Locate every Plasmodium falciparum-infected red blood cell.
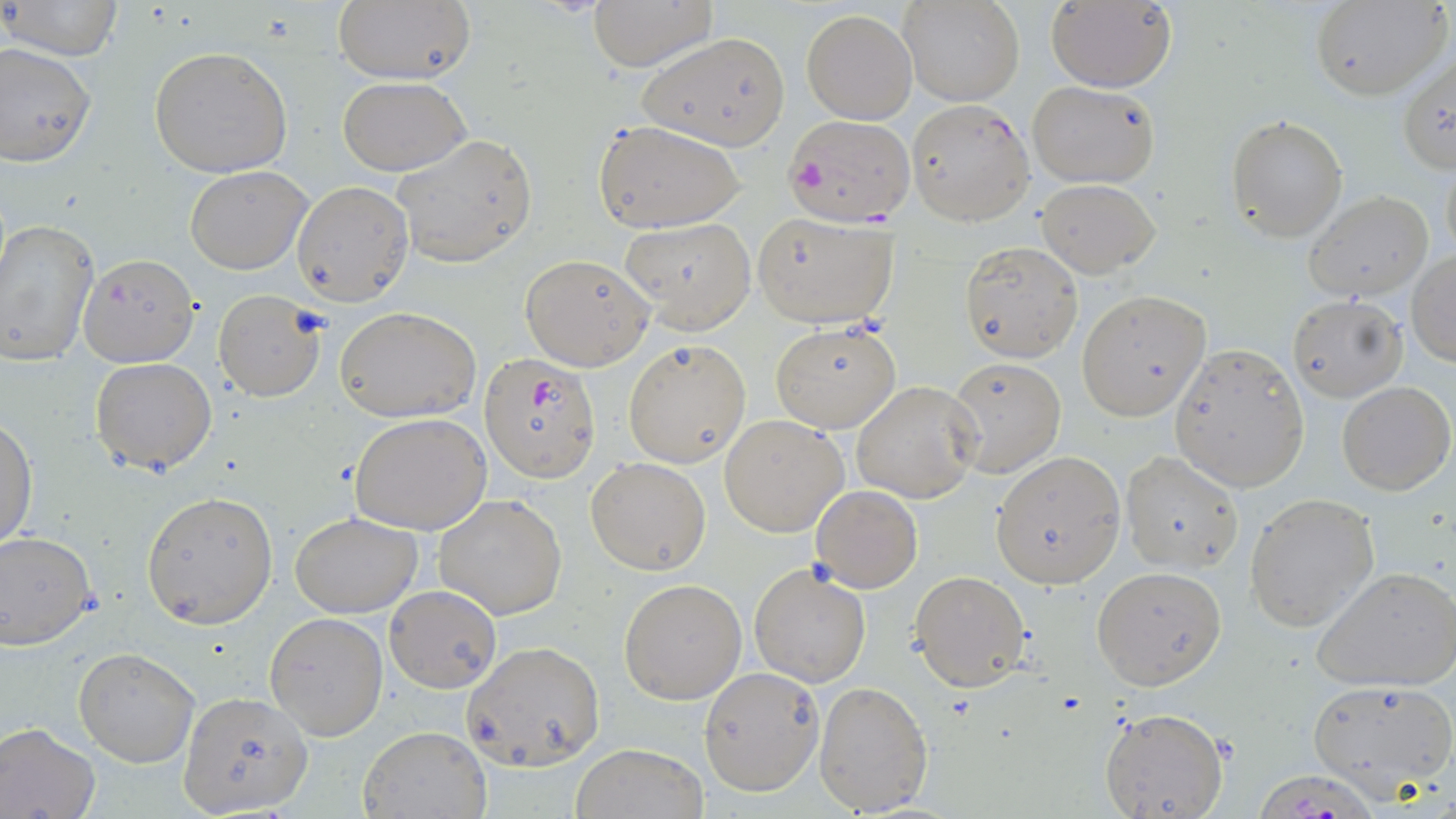

Approximate bounding boxes as (x1, y1, x2, y2) in pixels.
Plasmodium falciparum-infected red blood cells: (906, 99, 1034, 227), (783, 114, 915, 227), (480, 354, 600, 483).

Uninfected red blood cell locations: (330, 0, 477, 87), (584, 0, 718, 70), (901, 0, 1024, 107), (1309, 0, 1450, 102), (2, 1, 126, 62), (1045, 1, 1177, 91), (801, 7, 917, 125), (637, 30, 792, 152), (0, 42, 97, 166), (149, 44, 294, 177), (1397, 49, 1456, 176), (337, 76, 470, 175), (1026, 79, 1160, 188), (1226, 115, 1348, 241), (594, 120, 744, 233), (392, 133, 537, 268), (1440, 154, 1455, 265), (185, 166, 311, 274), (1037, 179, 1160, 276), (292, 180, 415, 305), (1304, 191, 1434, 302), (752, 211, 898, 329), (620, 218, 756, 332), (0, 219, 99, 369), (959, 240, 1084, 362), (1408, 250, 1456, 365), (78, 251, 199, 368), (519, 253, 654, 372), (213, 288, 326, 401), (1076, 290, 1211, 420), (1286, 294, 1405, 402), (334, 306, 480, 423), (769, 321, 902, 433), (622, 337, 751, 467), (1170, 345, 1310, 492), (90, 357, 218, 474), (947, 357, 1065, 477), (850, 380, 982, 502), (1338, 380, 1454, 496), (719, 413, 849, 537), (351, 414, 493, 534), (0, 419, 37, 552), (991, 451, 1124, 587), (1120, 451, 1245, 573), (585, 456, 712, 574), (811, 486, 924, 592), (141, 491, 278, 628), (1245, 493, 1380, 632), (431, 494, 569, 621), (289, 511, 422, 618), (0, 532, 98, 648), (749, 562, 872, 686), (1091, 566, 1227, 689), (1313, 566, 1456, 692), (910, 570, 1031, 691), (619, 577, 748, 704), (384, 584, 501, 695), (263, 611, 387, 740), (462, 640, 606, 770), (73, 646, 201, 767), (698, 665, 825, 798), (1303, 676, 1456, 798), (813, 678, 934, 816), (176, 691, 314, 816), (1098, 707, 1229, 819), (0, 723, 100, 819), (359, 726, 490, 818), (572, 741, 707, 818). Slide-level diagnosis: Plasmodium falciparum. Optical microscopy. 1000x magnification. Image is 1456×819 pixels. May-Grünwald-Giemsa stain. Thin blood smear. One field of a larger specimen.